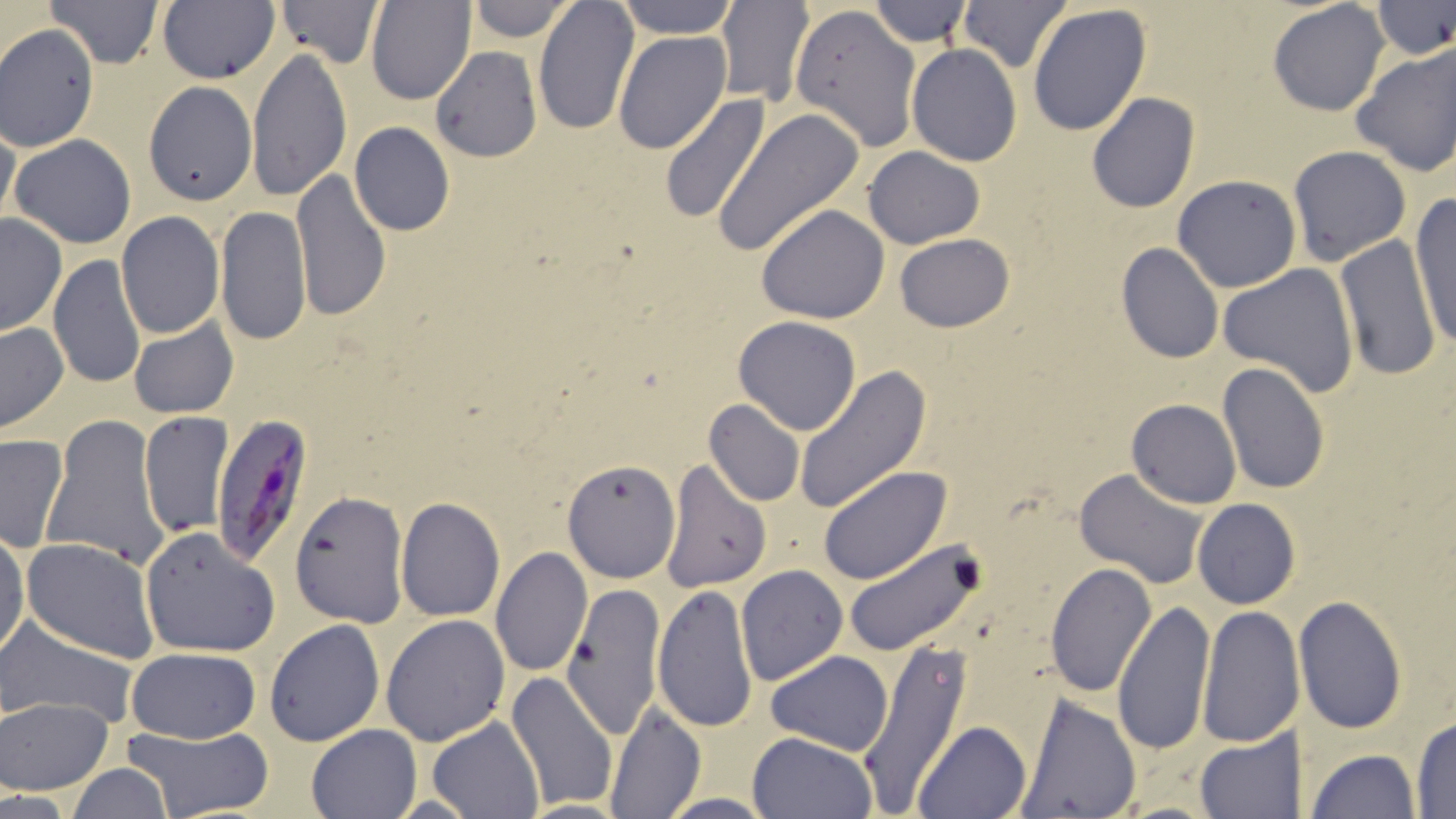

slide-level diagnosis = Plasmodium falciparum
field of view = single
image size = 1456×819 pixels
preparation = thin blood smear
uninfected red blood cell locations = approximate bounding boxes as (x1,y1)-(x2,y2) corner pairs in pixels: (43,0)-(164,69), (157,0)-(278,85), (274,0)-(385,69), (367,0)-(475,105), (466,0)-(576,42), (532,0)-(640,135), (614,0)-(740,38), (716,0)-(815,108), (956,0)-(1072,73), (869,1)-(972,49), (1267,1)-(1390,116), (1027,3)-(1152,138), (1372,3)-(1456,58), (790,4)-(922,153), (0,24)-(99,152), (613,32)-(731,154), (906,44)-(1023,166), (1350,44)-(1456,178), (246,47)-(352,202), (430,47)-(541,162), (145,81)-(255,206), (1086,93)-(1200,213), (659,94)-(772,225), (714,109)-(863,254), (0,115)-(20,233), (350,122)-(455,236), (309,128)-(434,275), (9,134)-(137,249), (1286,145)-(1411,265), (863,146)-(985,249), (291,168)-(391,322), (1172,174)-(1302,293), (1408,195)-(1456,351), (756,203)-(889,323), (216,207)-(311,346), (116,212)-(224,338), (1,213)-(67,337), (893,233)-(1016,332), (1336,233)-(1440,381), (1116,242)-(1224,364), (48,254)-(147,393), (1217,264)-(1361,396), (733,316)-(862,436), (128,318)-(238,420), (0,323)-(69,435), (1216,363)-(1330,494), (794,367)-(931,515), (1127,399)-(1241,507), (703,400)-(805,506), (139,410)-(233,537), (41,412)-(169,569), (0,435)-(69,552), (664,456)-(770,592), (562,460)-(681,583), (817,466)-(952,586), (1074,469)-(1208,587), (287,490)-(410,628), (397,497)-(505,622), (1192,498)-(1300,610), (140,526)-(280,657), (0,530)-(28,663), (23,539)-(159,662), (843,539)-(983,657), (491,547)-(591,678), (1045,562)-(1157,697), (736,564)-(849,686), (561,580)-(667,737), (653,583)-(757,733), (1294,595)-(1408,734), (1111,597)-(1217,757), (1196,603)-(1302,749), (380,613)-(510,745), (0,615)-(138,728), (264,620)-(385,748), (855,641)-(975,810), (125,648)-(262,743), (766,650)-(893,754), (506,672)-(619,810), (1018,693)-(1142,819), (1,697)-(113,795), (603,701)-(704,818), (1410,714)-(1455,816), (427,717)-(543,819), (915,719)-(1032,818), (124,724)-(275,817), (305,724)-(422,817), (1195,730)-(1302,817), (746,731)-(876,819), (1306,748)-(1421,819), (67,764)-(175,818), (656,794)-(780,817), (516,800)-(630,817)
magnification = 1000x
stain = May-Grünwald-Giemsa
Plasmodium falciparum-infected red blood cell locations = approximate bounding boxes as (x1,y1)-(x2,y2) corner pairs in pixels: (211,417)-(318,573)
modality = optical microscopy